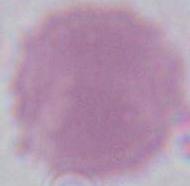
Summary:
  - Modality: micrograph
  - Magnification: 1000x
  - Identification: red blood cell